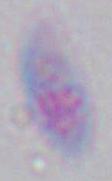
{
  "modality": "micrograph",
  "identification": "Toxoplasma gondii",
  "magnification": "1000x"
}